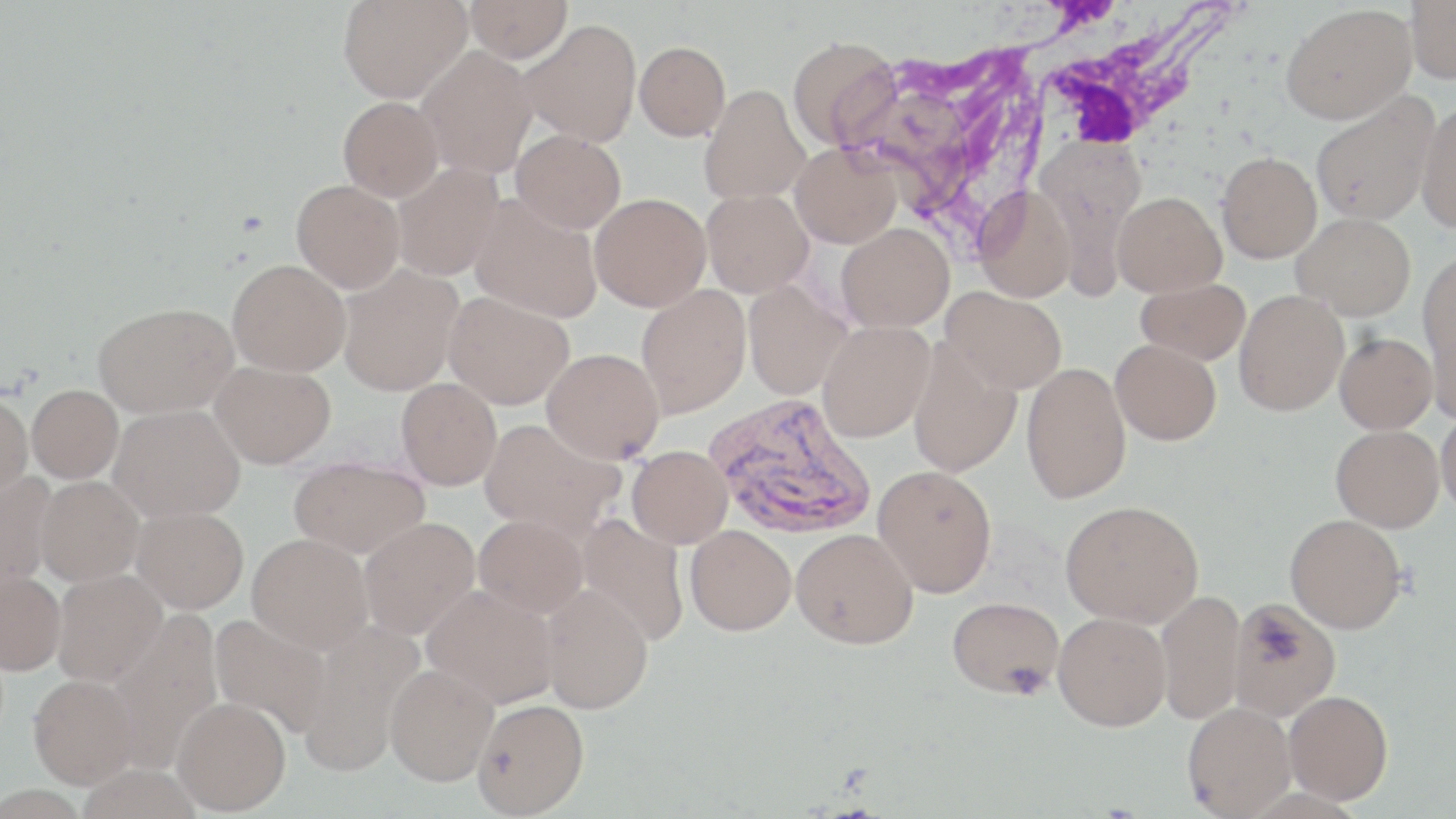
slide-level diagnosis = Plasmodium vivax
preparation = thin blood smear
stain = May-Grünwald-Giemsa
uninfected red blood cell locations = approximate bounding boxes as (x1,y1)-(x2,y2) corner pairs in pixels: (337,0)-(472,103), (465,0)-(573,62), (1406,0)-(1456,84), (1281,4)-(1416,123), (519,19)-(642,147), (787,36)-(901,152), (634,42)-(730,141), (415,46)-(537,178), (699,85)-(810,205), (881,86)-(973,220), (1310,93)-(1439,225), (338,96)-(443,201), (1416,101)-(1456,233), (511,129)-(626,233), (790,143)-(901,248), (1216,152)-(1321,263), (392,163)-(503,281), (291,179)-(405,293), (973,184)-(1077,302), (701,189)-(813,297), (1113,192)-(1226,297), (589,193)-(711,311), (470,195)-(603,323), (1292,213)-(1415,320), (837,223)-(954,332), (1418,254)-(1456,365), (227,258)-(350,376), (338,265)-(463,395), (1136,278)-(1251,365), (743,281)-(850,400), (636,285)-(751,418), (941,287)-(1067,394), (1234,290)-(1349,416), (444,291)-(575,409), (94,302)-(238,417), (1425,316)-(1456,426), (817,321)-(934,442), (1334,332)-(1437,434), (907,339)-(1021,477), (1110,339)-(1221,445), (542,348)-(665,463), (210,361)-(336,468), (1021,362)-(1131,504), (396,378)-(502,490), (27,385)-(124,484), (0,394)-(33,504), (109,404)-(245,522), (1436,410)-(1456,515), (479,418)-(625,540), (1331,425)-(1444,533), (627,446)-(733,547), (288,456)-(429,558), (873,465)-(997,597), (0,472)-(57,599), (35,477)-(144,587), (1061,500)-(1204,627), (131,506)-(249,614), (1285,513)-(1406,633), (474,514)-(588,618), (574,514)-(690,647), (359,517)-(480,639), (685,525)-(796,636), (791,528)-(918,649), (247,533)-(373,653), (51,568)-(167,685), (0,573)-(66,676), (421,584)-(559,708), (539,585)-(654,714), (1156,589)-(1246,724), (1229,596)-(1341,721), (948,597)-(1064,698), (103,611)-(224,770), (1053,612)-(1171,730), (210,614)-(333,738), (294,621)-(424,776), (386,662)-(499,786), (28,676)-(140,791), (1284,690)-(1394,805), (173,697)-(291,815), (472,698)-(590,818), (1182,701)-(1295,818)
Plasmodium vivax-infected red blood cell locations = approximate bounding boxes as (x1,y1)-(x2,y2) corner pairs in pixels: (704,394)-(877,540)
field of view = one of a larger specimen
magnification = 1000x
white blood cell locations = approximate bounding boxes as (x1,y1)-(x2,y2) corner pairs in pixels: (1007,1)-(1244,157)
image size = 1456×819 pixels
modality = optical microscopy